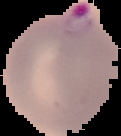

Result: malaria parasites identified. Cell region segmented out of the field of view; the surrounding area is masked to black. From a thin blood film. Image is 121×136 pixels.